Locate every uninfected red blood cell.
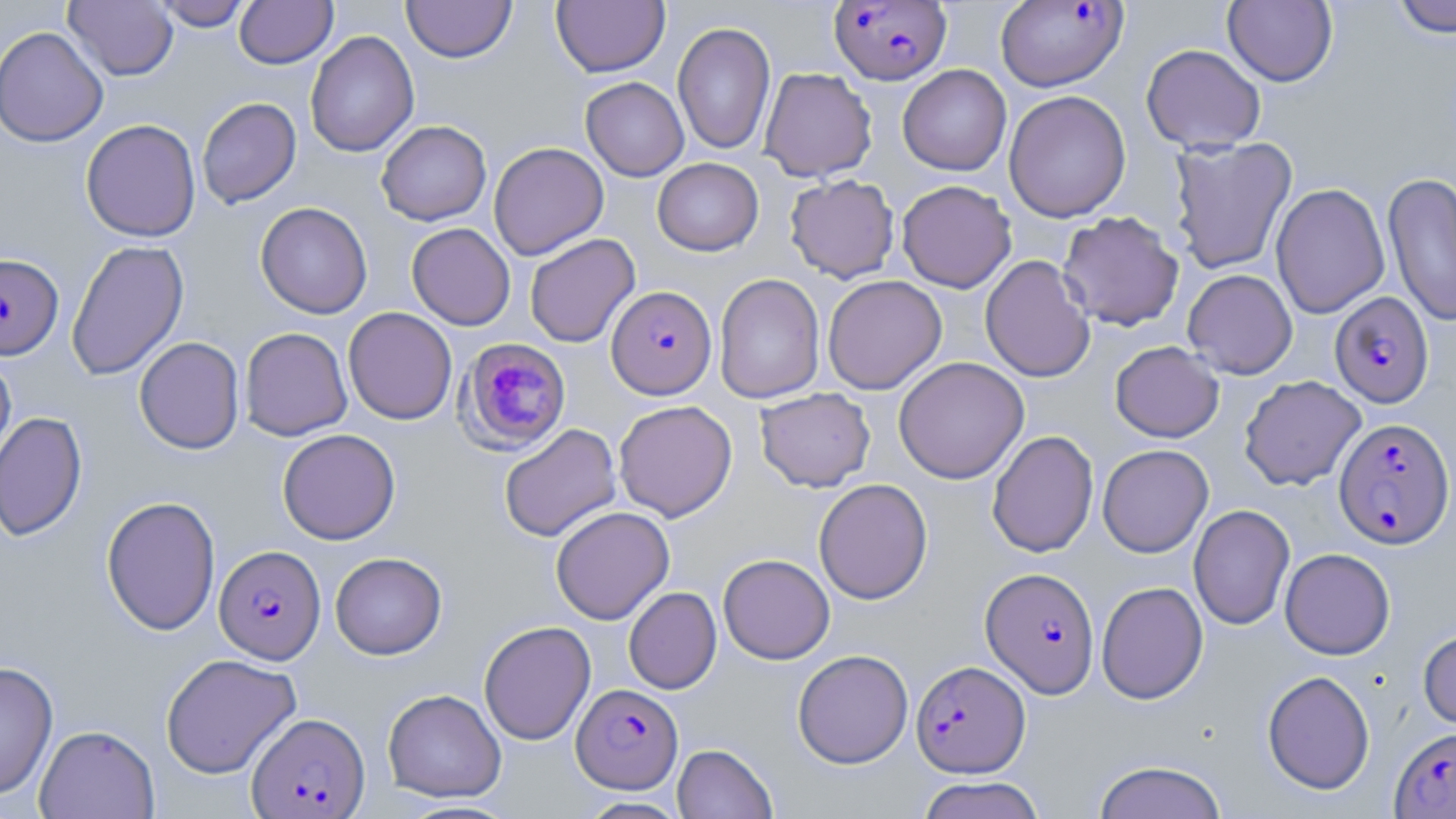

Approximate bounding boxes as named x1/y1/x2/y2 corners in pixels.
Uninfected red blood cells: (x1=65, y1=0, x2=178, y2=81), (x1=152, y1=0, x2=253, y2=30), (x1=234, y1=0, x2=338, y2=68), (x1=402, y1=0, x2=516, y2=63), (x1=1389, y1=0, x2=1455, y2=38), (x1=552, y1=1, x2=670, y2=77), (x1=1223, y1=1, x2=1338, y2=87), (x1=672, y1=21, x2=776, y2=156), (x1=0, y1=26, x2=109, y2=147), (x1=305, y1=30, x2=419, y2=158), (x1=1141, y1=43, x2=1266, y2=153), (x1=897, y1=64, x2=1011, y2=175), (x1=759, y1=67, x2=877, y2=181), (x1=580, y1=77, x2=689, y2=181), (x1=1004, y1=90, x2=1131, y2=223), (x1=197, y1=97, x2=301, y2=208), (x1=81, y1=118, x2=201, y2=242), (x1=376, y1=120, x2=491, y2=226), (x1=1168, y1=136, x2=1298, y2=275), (x1=488, y1=141, x2=609, y2=260), (x1=652, y1=157, x2=763, y2=256), (x1=1382, y1=171, x2=1456, y2=328), (x1=785, y1=174, x2=900, y2=283), (x1=897, y1=180, x2=1017, y2=293), (x1=1271, y1=183, x2=1390, y2=318), (x1=255, y1=201, x2=373, y2=319), (x1=1057, y1=210, x2=1184, y2=331), (x1=407, y1=223, x2=516, y2=330), (x1=524, y1=233, x2=640, y2=348), (x1=66, y1=239, x2=189, y2=381), (x1=980, y1=255, x2=1095, y2=383), (x1=1182, y1=268, x2=1298, y2=379), (x1=714, y1=273, x2=825, y2=404), (x1=822, y1=275, x2=947, y2=395), (x1=343, y1=307, x2=457, y2=425), (x1=239, y1=327, x2=352, y2=441), (x1=134, y1=337, x2=245, y2=454), (x1=1110, y1=341, x2=1224, y2=443), (x1=0, y1=352, x2=16, y2=470), (x1=893, y1=356, x2=1029, y2=484), (x1=1239, y1=375, x2=1366, y2=491), (x1=755, y1=388, x2=875, y2=492), (x1=613, y1=400, x2=737, y2=521), (x1=0, y1=411, x2=87, y2=542), (x1=499, y1=423, x2=621, y2=542), (x1=277, y1=429, x2=400, y2=544), (x1=987, y1=430, x2=1099, y2=558), (x1=1097, y1=444, x2=1213, y2=557), (x1=813, y1=478, x2=933, y2=604), (x1=101, y1=495, x2=220, y2=635), (x1=1188, y1=504, x2=1295, y2=630), (x1=550, y1=506, x2=675, y2=625), (x1=1280, y1=548, x2=1395, y2=659), (x1=330, y1=552, x2=447, y2=659), (x1=718, y1=553, x2=835, y2=664), (x1=1096, y1=581, x2=1208, y2=704), (x1=623, y1=586, x2=722, y2=694), (x1=479, y1=620, x2=596, y2=745), (x1=1418, y1=627, x2=1456, y2=730), (x1=792, y1=649, x2=913, y2=769), (x1=160, y1=653, x2=301, y2=778), (x1=0, y1=660, x2=58, y2=799), (x1=1262, y1=670, x2=1375, y2=794), (x1=382, y1=688, x2=506, y2=802), (x1=34, y1=724, x2=160, y2=819), (x1=672, y1=743, x2=777, y2=818), (x1=1092, y1=760, x2=1228, y2=819), (x1=916, y1=775, x2=1047, y2=819), (x1=576, y1=796, x2=691, y2=818).

Plasmodium falciparum-infected red blood cell locations: (x1=830, y1=1, x2=951, y2=85), (x1=996, y1=1, x2=1128, y2=92), (x1=0, y1=253, x2=63, y2=360), (x1=606, y1=285, x2=716, y2=399), (x1=1330, y1=292, x2=1433, y2=408), (x1=457, y1=338, x2=572, y2=454), (x1=1333, y1=417, x2=1455, y2=548), (x1=213, y1=544, x2=326, y2=664), (x1=981, y1=567, x2=1100, y2=697), (x1=911, y1=659, x2=1029, y2=777), (x1=572, y1=683, x2=683, y2=793), (x1=247, y1=712, x2=370, y2=818), (x1=1389, y1=726, x2=1456, y2=818). Slide-level diagnosis: Plasmodium falciparum. Captured at 1000x magnification. Image is 1456×819 pixels. One field of a larger specimen. Optical microscopy. Thin blood film. May-Grünwald-Giemsa stain.